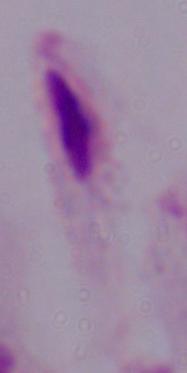
Summary:
  - Magnification: 1000x
  - Modality: micrograph
  - Identification: trichomonad